Locate every malaria parasite.
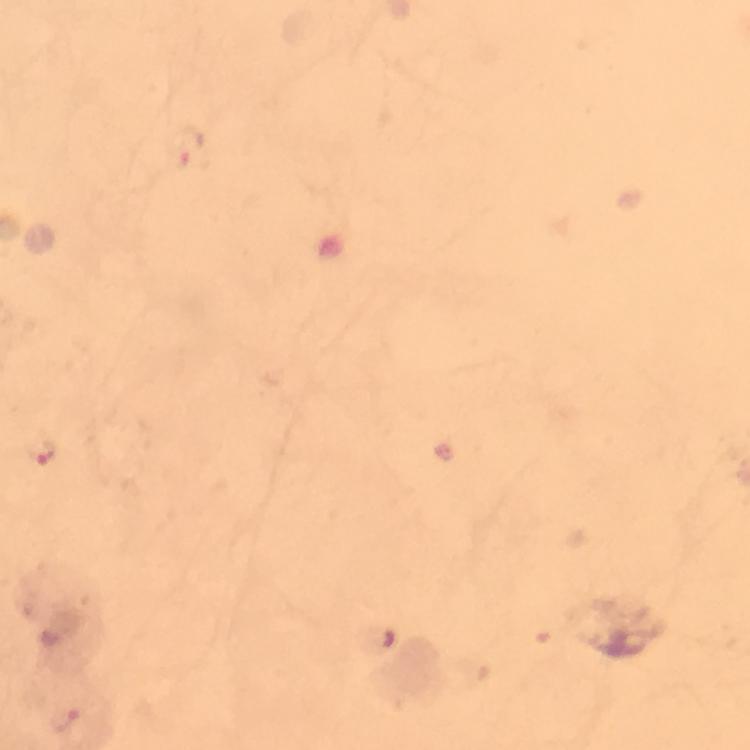
Approximate centers as (x, y) in pixels.
Malaria parasites: (43, 450).

Cropped region of a single field of view. Image is 750×750 pixels. Thick blood smear. From a diagnostic examination for malaria. Photographed through the microscope with a smartphone camera. Immersion oil applied. At 100x magnification. Giemsa stain.